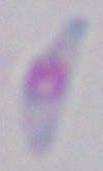
Summary:
  - Identification: Toxoplasma gondii
  - Magnification: 1000x
  - Modality: micrograph